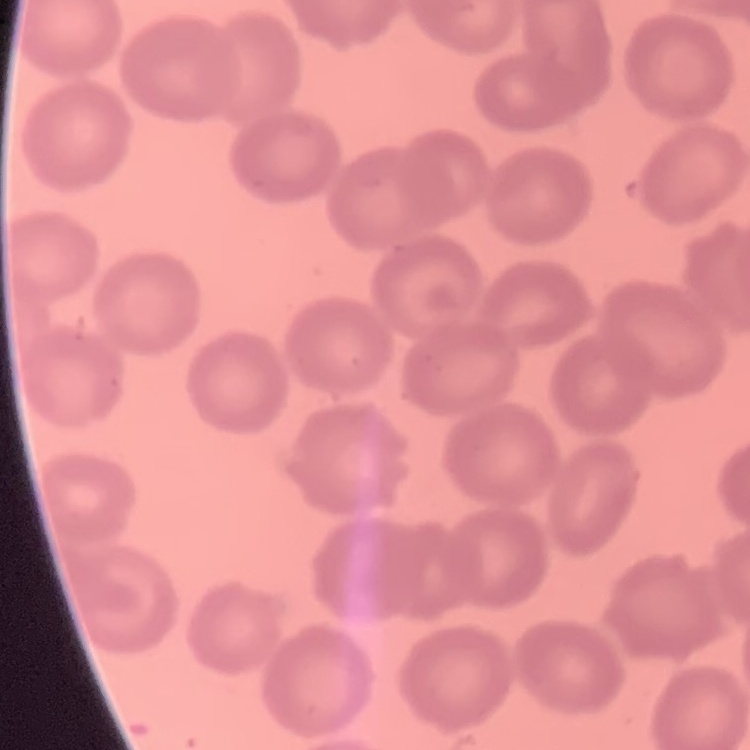
Summary:
  - Red blood cell morphology: no rouleaux formation
  - Preparation: thin blood film
  - Stain: Field's or Giemsa
  - Image type: one tile cut from a larger photomicrograph